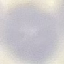
Malaria status: uninfected. Acquired by smartphone through the microscope eyepiece. Giemsa stain. Thin smear of blood. Automatically extracted cell patch, resized to 64 × 64 pixels.